Assess this cell for malaria.
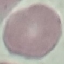
It is uninfected.

Summary:
  - Stain: Giemsa
  - Capture: smartphone camera at the microscope eyepiece
  - Preparation: thin blood film
  - Image type: cell patch, automatically extracted from a larger field of view and resized to 64 × 64 pixels